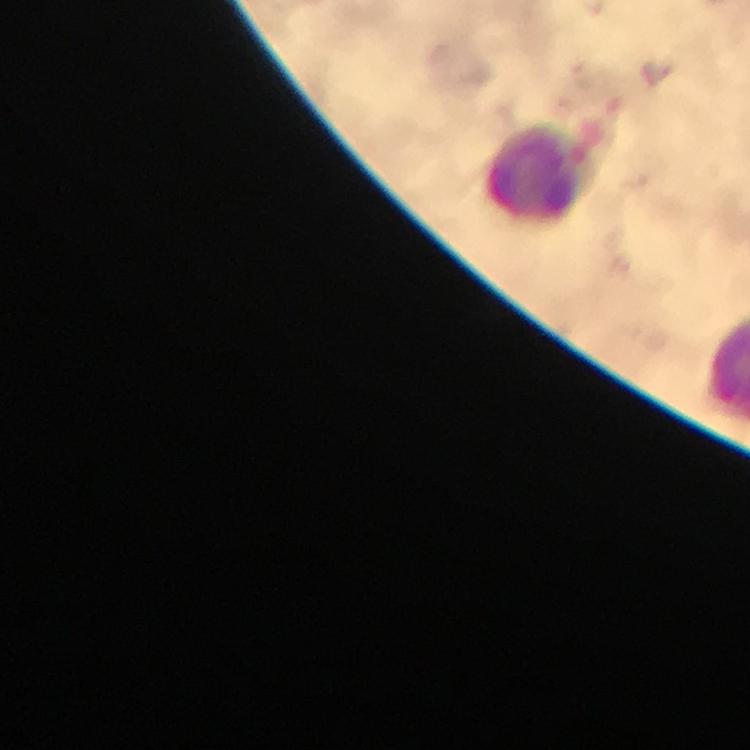

Approximate centers as (x, y) in pixels.
Summary:
  - Leukocyte locations: (540, 176)
  - Stain: Giemsa
  - Preparation: thick blood smear
  - Immersion oil: used
  - Cropped from: a single field of view
  - Capture: smartphone photograph through a microscope
  - Magnification: 100x
  - Malaria parasites: none detected
  - Image size: 750×750 pixels
  - Context: from a malaria diagnostic workup